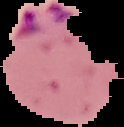
Image is 124×127 pixels. Cell region segmented out of the field of view; the surrounding area is masked to black. Result: Plasmodium parasites identified. From a thin blood smear.